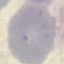
Malaria status: uninfected. Photographed with a smartphone camera at the microscope eyepiece. Thin smear of blood. Cell patch, automatically extracted from a larger field of view and resized to 64 × 64 pixels. Giemsa-stained preparation.